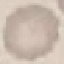 Malaria status: uninfected. Photographed with a smartphone camera at the microscope eyepiece. Automatically extracted cell patch, resized to 64 × 64 pixels. Thin blood smear. Giemsa stain.